Give the position of every leukocyte visible.
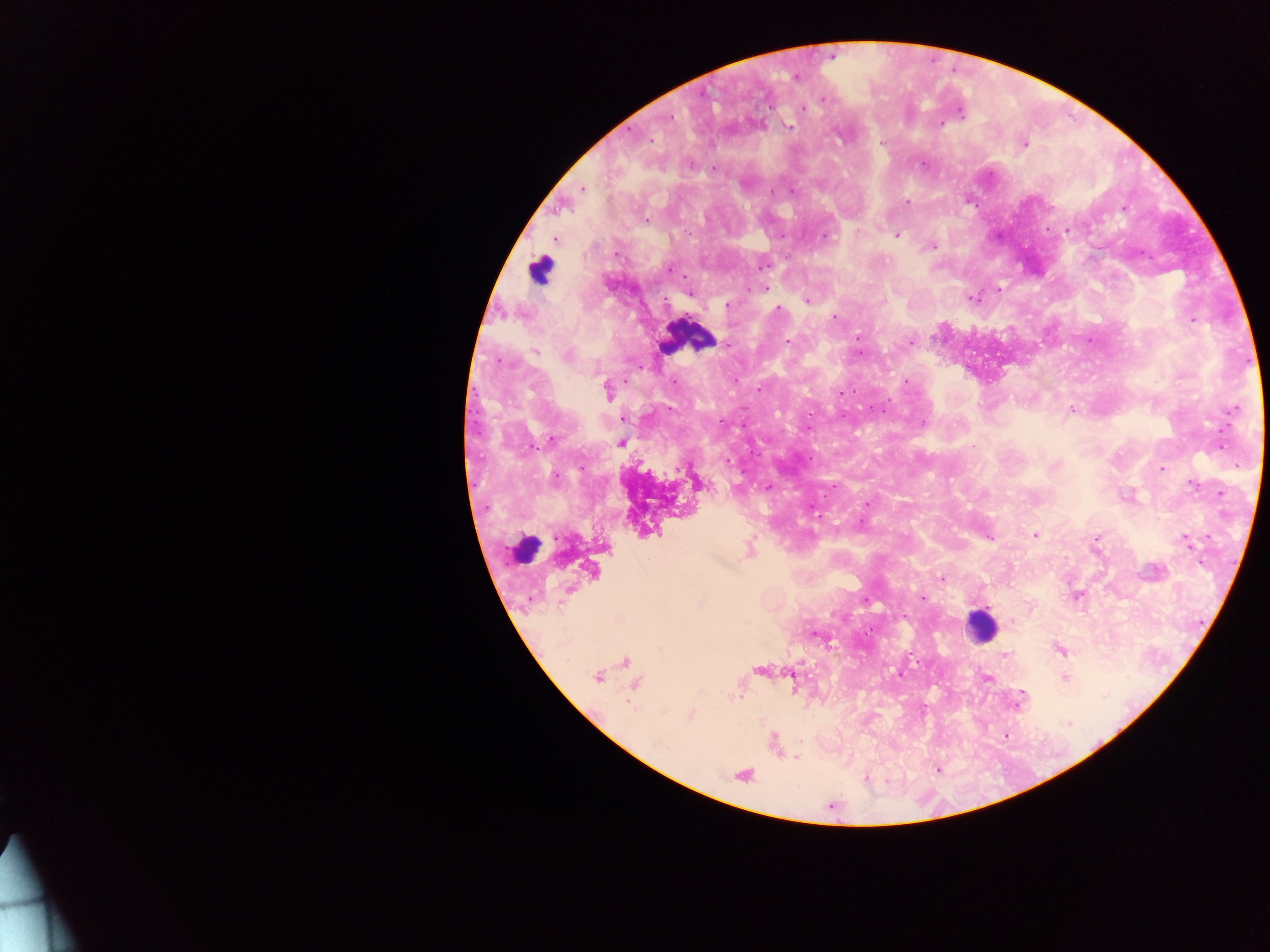

Approximate centers as x y in pixels.
Leukocytes: 540 270; 689 336; 524 549; 979 626.

preparation = thick blood film
malaria parasite locations = approximate centers as x y in pixels: 796 77; 822 99; 803 108; 669 117; 940 123; 787 126; 650 140; 1024 143; 922 163; 713 169; 582 188; 774 193; 906 202; 1123 208; 645 220; 1048 229; 1066 230; 896 235; 554 239; 931 245; 670 269; 765 288; 998 289; 689 292; 972 298; 807 301; 726 304; 777 310; 834 316; 1194 321; 726 342; 788 342; 909 342; 536 351; 858 352; 498 361; 906 380; 607 391; 1232 409; 1072 410; 623 418; 922 422; 550 439; 620 441; 727 463; 1162 469; 1191 483; 766 487; 1220 494; 866 504; 1034 534; 988 536; 1096 538; 1185 538; 748 549; 941 578; 1075 596; 922 598; 1029 607; 815 634; 1061 649; 1004 656; 625 662; 758 670; 900 672; 790 674; 1064 676; 597 677; 986 677; 634 683; 738 694; 1021 697; 690 715; 1005 735; 774 742; 795 756; 937 769; 742 774; 867 778
capture = mobile-phone photograph through a microscope
image size = 1270×952 pixels
field of view = single
country = Ghana